State the preparation type.
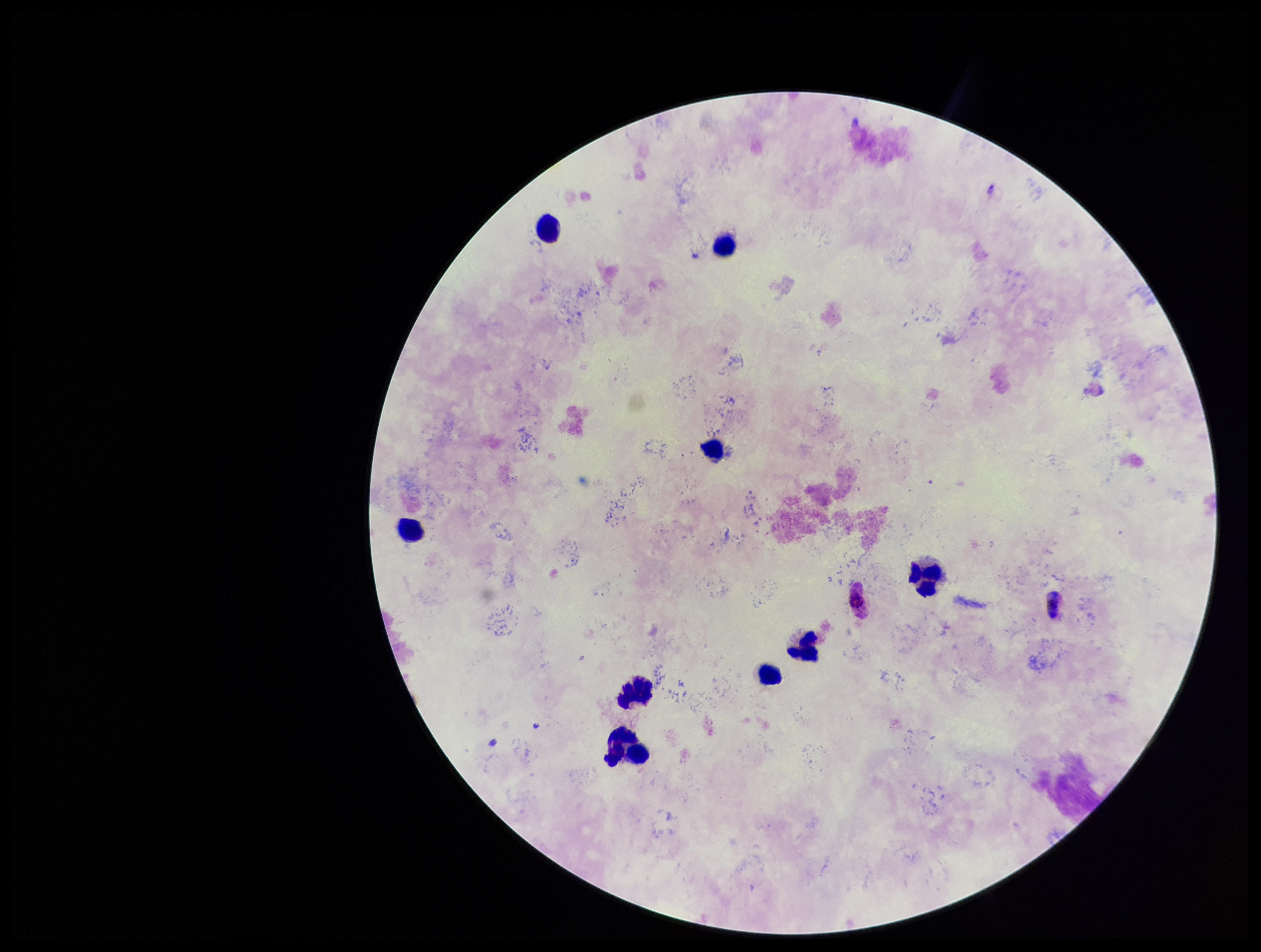

It is a thick blood smear.

Leukocyte count: 9. Parasite count: 0. Species reported for this patient: Plasmodium falciparum. Patient malaria status: positive. Stained with Giemsa. Plasmodium parasites: none identified. Single field of view. Smartphone photograph taken through the eyepiece of a microscope. Image is 1261×952 pixels.